Assess the morphology of the erythrocytes.
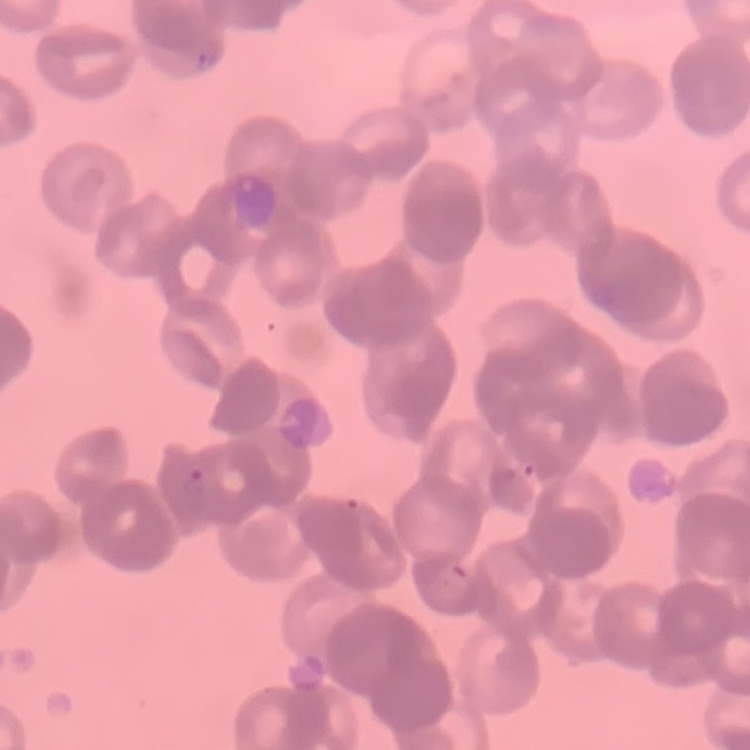

They show rouleaux formation.

{
  "preparation": "thin blood film",
  "stain": "Field's or Giemsa",
  "image_type": "square crop of a larger photomicrograph"
}